Assess this cell for malaria.
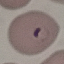

It is parasitized.

Photographed with a smartphone camera at the microscope eyepiece. Cell patch, automatically extracted from a larger field of view and resized to 64 × 64 pixels. Giemsa stain. Thin smear of blood.